State the blood parasite species.
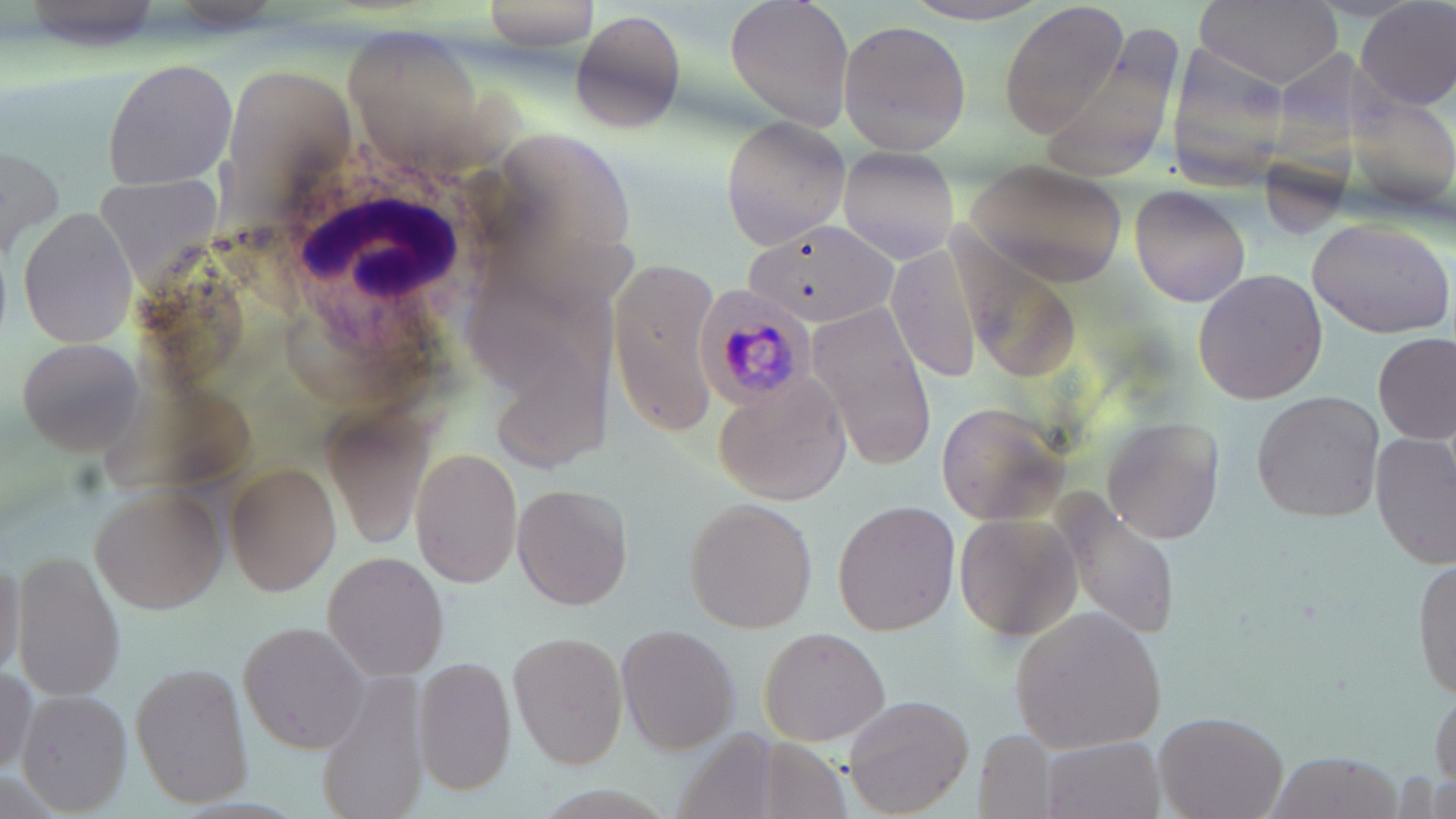

Plasmodium malariae.

Summary:
  - Coordinate format: approximate bounding boxes as (x1,y1)-(x2,y2) corner pairs in pixels
  - Plasmodium malariae-infected red blood cell locations: (694,283)-(818,413)
  - White blood cell locations: (246,149)-(513,352)
  - Uninfected red blood cell locations: (477,0)-(606,51), (725,0)-(852,133), (1192,0)-(1342,87), (1357,0)-(1456,111), (999,1)-(1130,137), (893,2)-(1059,26), (572,9)-(686,135), (837,19)-(970,156), (342,25)-(494,172), (100,56)-(239,189), (221,62)-(357,203), (719,115)-(848,250), (2,143)-(62,263), (838,145)-(958,264), (962,157)-(1130,287), (91,171)-(224,280), (1130,182)-(1253,308), (18,205)-(141,349), (1306,214)-(1453,340), (747,215)-(899,331), (886,242)-(988,385), (606,254)-(725,432), (1192,269)-(1327,405), (806,303)-(938,466), (1374,332)-(1453,445), (13,335)-(146,455), (713,368)-(851,505), (1251,390)-(1385,523), (935,400)-(1066,525), (321,407)-(435,546), (1103,416)-(1226,544), (1370,432)-(1455,566), (407,445)-(524,587), (223,461)-(342,595), (89,479)-(228,615), (510,480)-(635,611), (682,496)-(820,633), (1063,497)-(1177,643), (831,498)-(961,636), (951,507)-(1085,650), (0,543)-(24,689), (322,549)-(450,682), (11,550)-(126,702), (1413,557)-(1456,703), (1005,606)-(1171,755), (236,620)-(373,756), (615,622)-(742,756), (756,624)-(892,747), (507,631)-(628,768), (411,655)-(517,795), (130,660)-(254,807), (0,666)-(40,779), (315,672)-(435,819), (1429,685)-(1455,799), (16,688)-(136,816), (841,692)-(975,817), (1153,710)-(1289,819), (974,731)-(1054,818), (1038,735)-(1163,817), (1268,752)-(1401,818)
  - Magnification: 1000x
  - Stain: May-Grünwald-Giemsa
  - Preparation: thin blood film
  - Field of view: one of a larger specimen
  - Image size: 1456×819 pixels
  - Modality: light microscopy